Assess this cell for malaria.
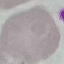

It is uninfected.

stain = Giemsa
preparation = thin smear
image type = cell patch, automatically extracted from a larger field of view and resized to 64 × 64 pixels
capture = smartphone through the microscope eyepiece